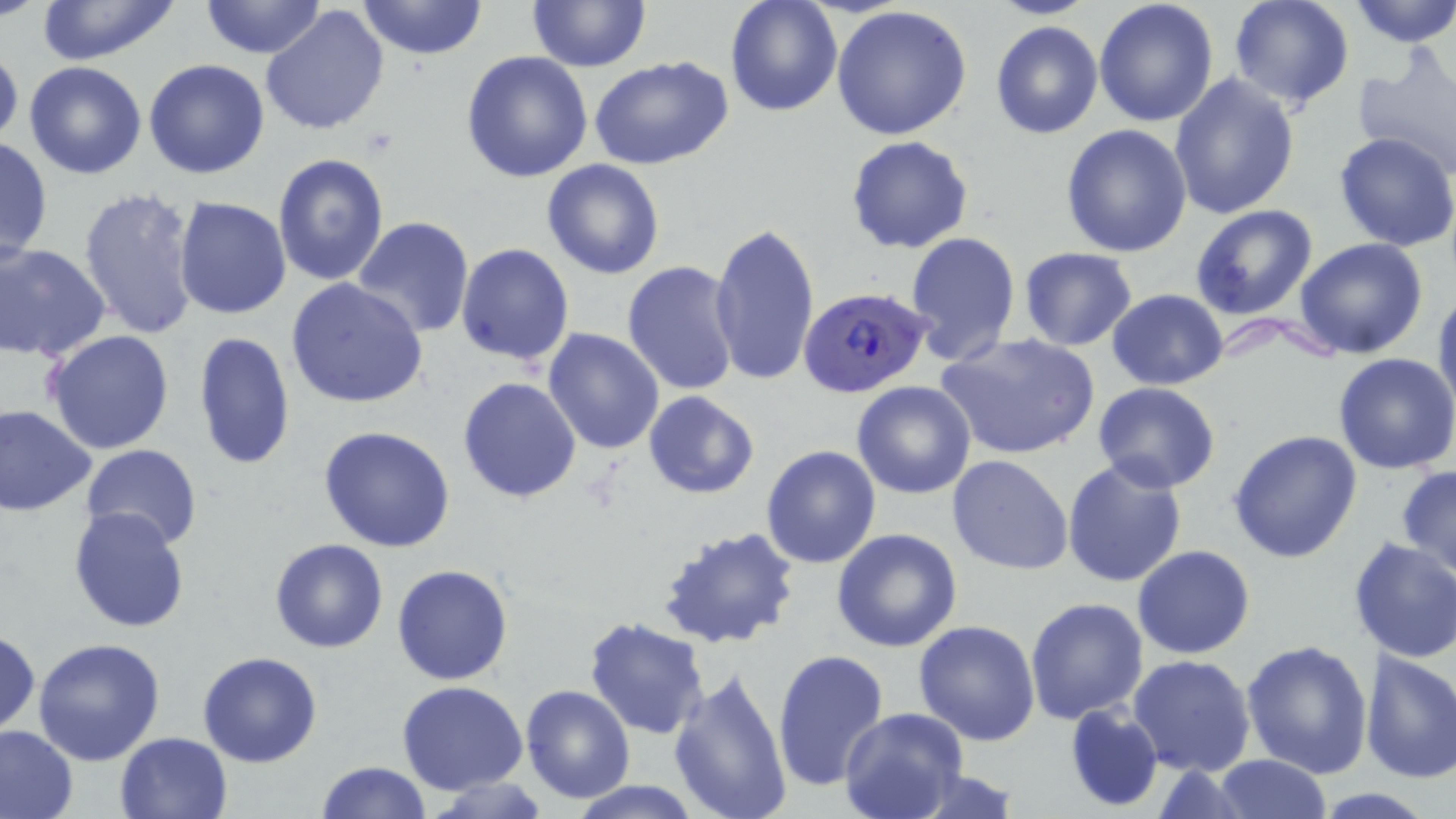

Approximate bounding boxes as (x1,y1)-(x2,y2) corner pairs in pixels. Plasmodium falciparum-infected red blood cell locations: (799,285)-(932,399). Uninfected red blood cell locations: (33,0)-(182,65), (199,0)-(327,60), (358,0)-(488,60), (528,0)-(651,72), (725,0)-(843,119), (1094,0)-(1220,127), (1227,0)-(1355,110), (1346,0)-(1456,47), (830,5)-(973,142), (260,6)-(388,136), (990,21)-(1103,138), (0,45)-(23,148), (460,50)-(592,183), (1352,51)-(1456,175), (589,55)-(737,170), (144,59)-(270,180), (24,61)-(148,180), (1168,73)-(1300,219), (1060,123)-(1192,257), (1333,131)-(1456,253), (846,135)-(975,255), (0,136)-(53,264), (273,152)-(390,288), (542,158)-(667,279), (79,185)-(201,338), (173,197)-(291,320), (1190,204)-(1319,321), (349,217)-(475,338), (707,219)-(819,387), (904,232)-(1022,364), (1294,238)-(1428,359), (1,242)-(109,361), (457,244)-(574,367), (1017,247)-(1138,350), (621,260)-(741,396), (285,277)-(429,410), (1433,287)-(1456,420), (1107,288)-(1229,390), (543,328)-(665,455), (42,330)-(176,455), (192,330)-(294,471), (935,332)-(1101,462), (1334,353)-(1456,476), (458,376)-(581,502), (851,381)-(978,499), (1093,382)-(1220,493), (643,391)-(759,498), (0,403)-(98,518), (319,425)-(456,552), (1229,430)-(1363,563), (762,444)-(883,569), (79,445)-(203,552), (947,455)-(1073,575), (1061,459)-(1188,589), (1397,466)-(1456,580), (68,507)-(191,634), (657,522)-(803,650), (832,527)-(963,651), (269,538)-(390,654), (1352,538)-(1456,663), (1133,544)-(1255,659), (391,564)-(514,684), (1025,596)-(1148,723), (584,616)-(709,738), (913,620)-(1041,746), (0,628)-(40,740), (31,637)-(166,765), (1241,639)-(1373,778), (772,650)-(890,793), (1360,650)-(1456,785), (197,651)-(323,768), (1129,654)-(1256,776), (668,665)-(793,819), (397,681)-(528,794), (519,685)-(635,803), (1064,703)-(1162,813), (838,708)-(968,819), (0,723)-(79,819), (114,731)-(233,819), (1212,754)-(1333,819), (316,760)-(432,818), (901,766)-(1021,819), (424,776)-(555,818), (571,780)-(703,819). Slide-level diagnosis: Plasmodium falciparum. May-Grünwald-Giemsa stain. Single field of view. Thin blood film. Image is 1456×819 pixels. Light microscopy. 1000x magnification.